Assess for Plasmodium parasites.
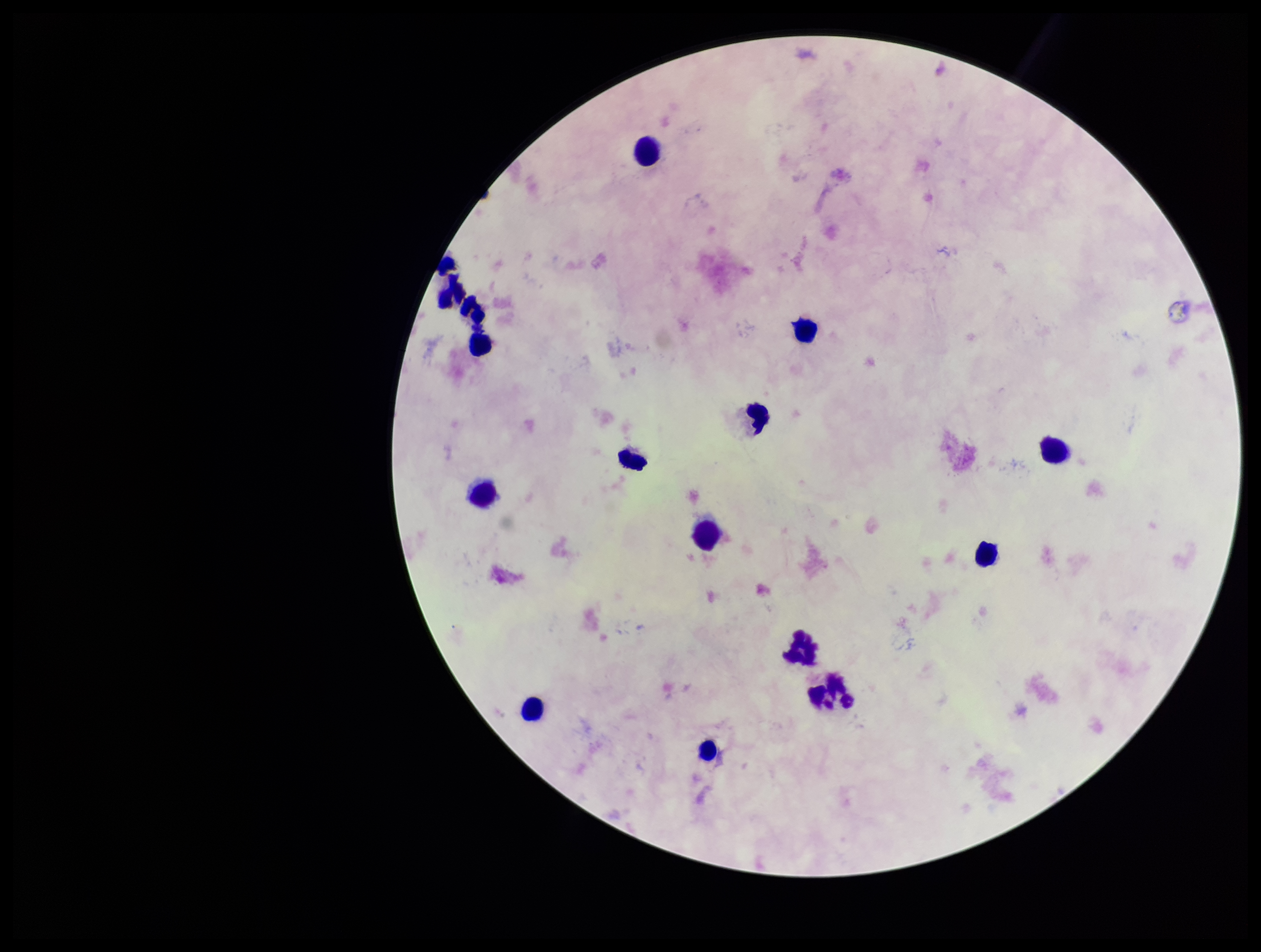

None detected.

Single field of view. Parasite count: 0. Preparation: thick blood smear. Photographed through the microscope eyepiece with a smartphone camera. Leukocyte count: 15. Image is 1261×952 pixels. Stained with Giemsa. Patient malaria status: negative.